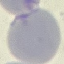 Malaria status: uninfected. Automatically extracted cell patch, resized to 64 × 64 pixels. Thin blood smear. Acquired by smartphone through the microscope eyepiece. Giemsa stain.